Identify the parasite.
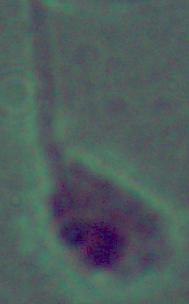

Leishmania.

Photomicrograph. Captured at 1000x magnification.